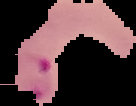

Image is 136×106 pixels. Malaria status: parasitized. From a thin blood smear. The area outside the segmented cell region is set to black.